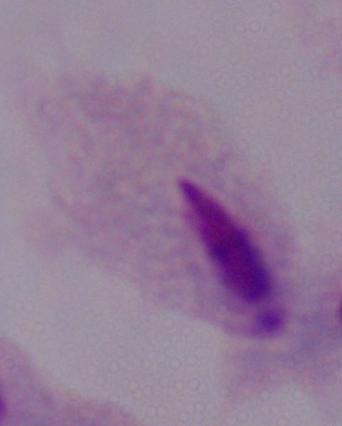

identification = trichomonad
magnification = 1000x
modality = micrograph